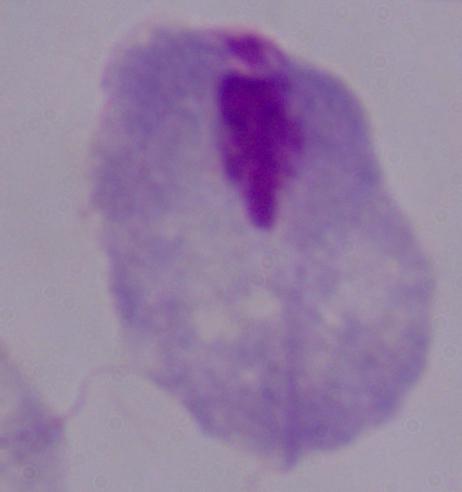

A trichomonad is shown. Captured at 1000x magnification. Micrograph.